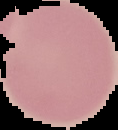 The area outside the segmented cell region is set to black. Result: negative for malaria parasites. Image is 118×130 pixels. From a thin blood smear.